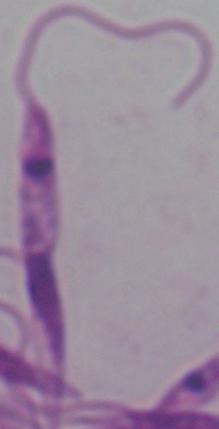

Summary:
  - Magnification: 1000x
  - Modality: photomicrograph
  - Identification: Leishmania